Assess this cell for malaria.
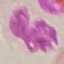

Uninfected.

Summary:
  - Image type: cell patch, automatically extracted from a larger field of view and resized to 64 × 64 pixels
  - Stain: Giemsa
  - Preparation: thin smear
  - Capture: smartphone camera at the microscope eyepiece